Describe the morphology of the red blood cells.
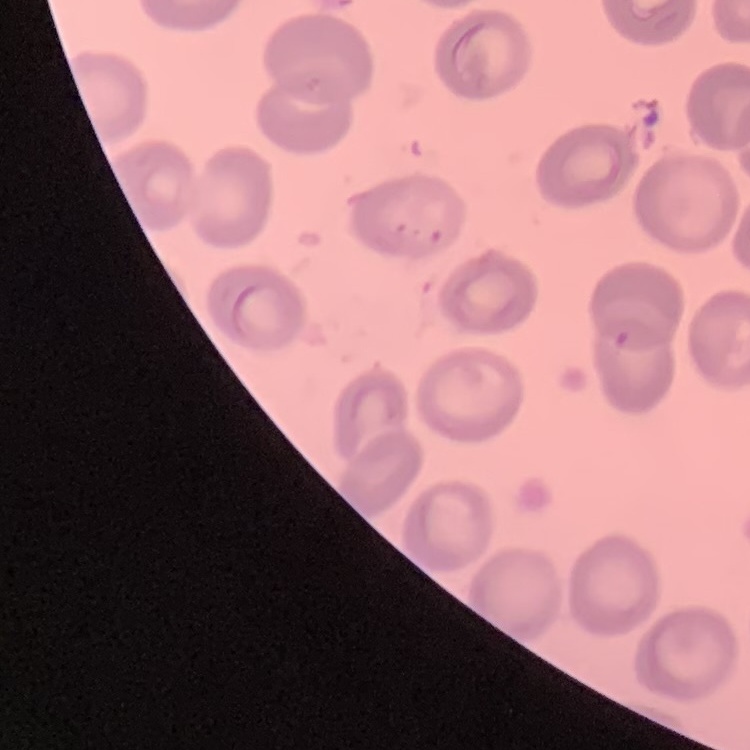
They show no rouleaux formation.

Summary:
  - Preparation: thin blood film
  - Image type: one tile cut from a larger photomicrograph
  - Stain: Field's or Giemsa